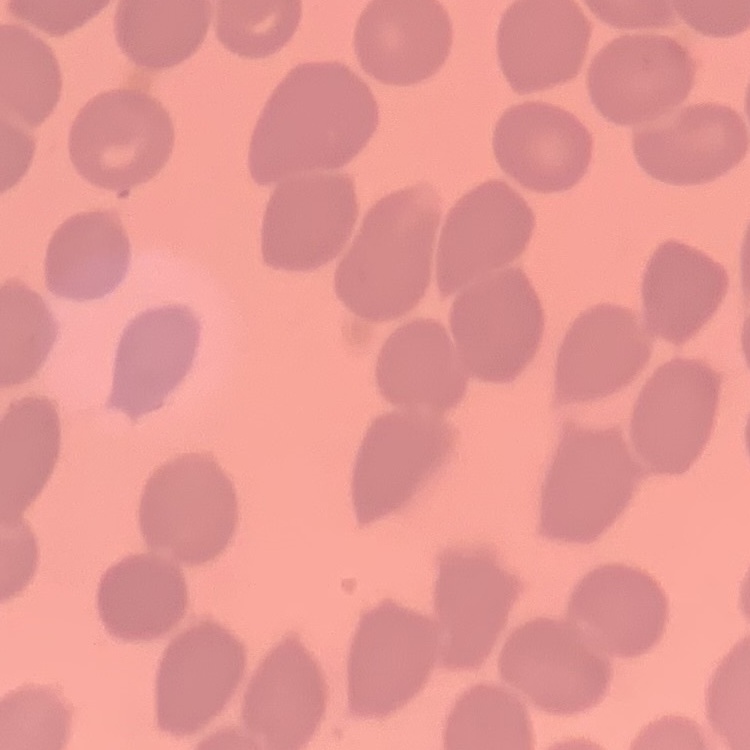

Summary:
  - Erythrocyte morphology: no rouleaux formation
  - Preparation: thin peripheral smear
  - Image type: one tile cut from a larger photomicrograph
  - Stain: Field's or Giemsa